Identify the cell.
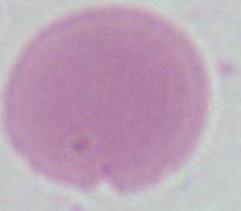
This is an erythrocyte.

Micrograph. 1000x magnification.